Locate every Plasmodium falciparum-infected red blood cell.
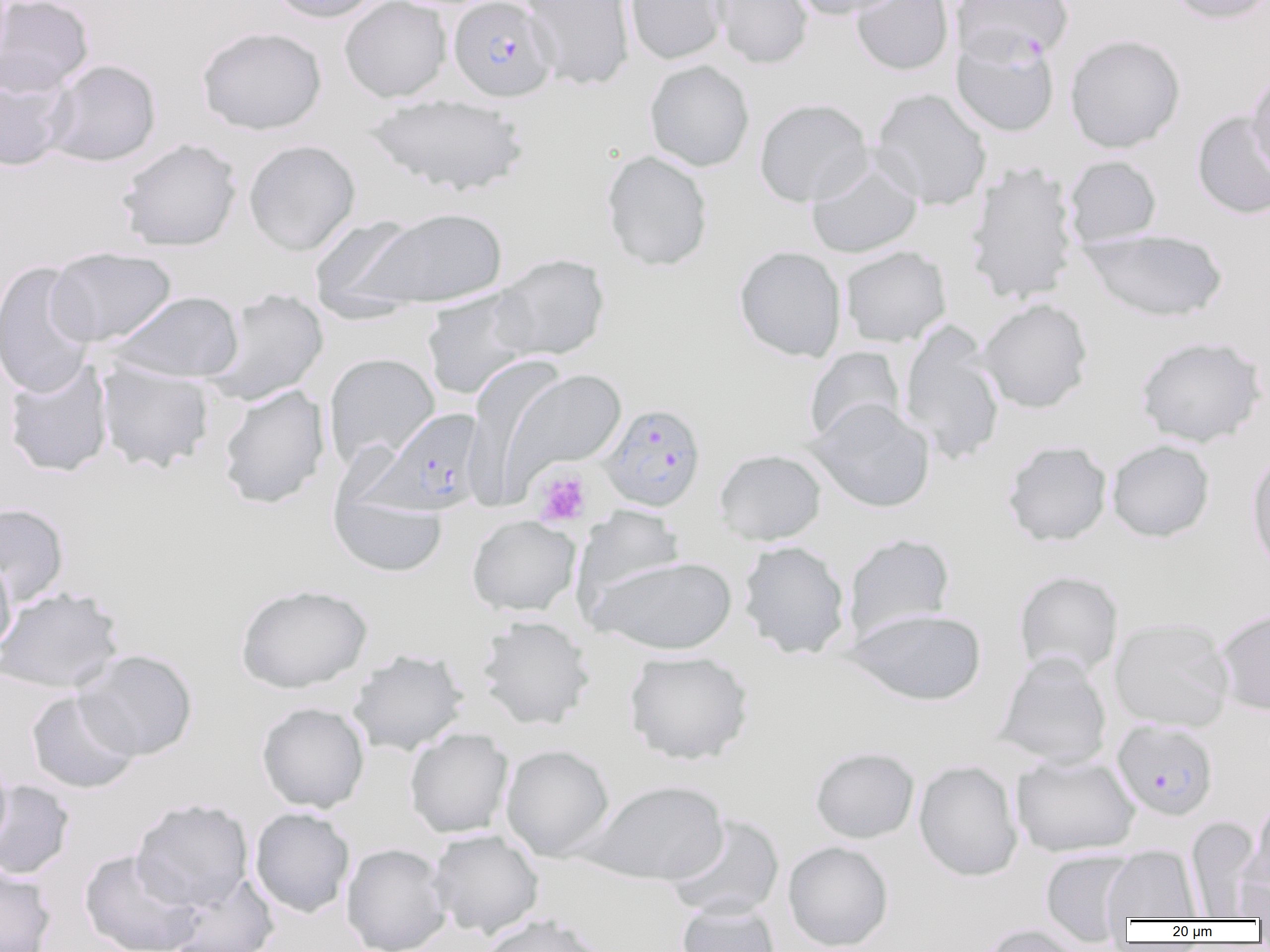

Approximate bounding boxes as (x1, y1, x2, y2) in pixels.
Plasmodium falciparum-infected red blood cells: (448, 0, 558, 102), (951, 30, 1060, 137), (598, 403, 707, 512), (368, 408, 487, 516), (1112, 719, 1219, 821).

{
  "slide_level_diagnosis": "Plasmodium falciparum",
  "platelet_locations": "approximate bounding boxes as (x1, y1, x2, y2) in pixels: (533, 468, 592, 526)",
  "magnification": "1000x",
  "image_size": "1270×952 pixels",
  "modality": "light microscopy",
  "field_of_view": "one of a larger specimen",
  "preparation": "thin blood smear",
  "uninfected_red_blood_cell_locations": "approximate bounding boxes as (x1, y1, x2, y2) in pixels: (0, 0, 94, 97), (266, 0, 383, 23), (339, 0, 452, 102), (522, 0, 636, 90), (623, 0, 730, 65), (711, 0, 814, 69), (788, 0, 907, 20), (851, 0, 954, 76), (952, 0, 1072, 49), (1164, 0, 1269, 25), (197, 26, 327, 135), (1065, 34, 1185, 152), (43, 59, 161, 167), (644, 60, 755, 171), (1246, 70, 1270, 181), (0, 71, 71, 171), (871, 88, 992, 211), (364, 94, 530, 196), (754, 98, 873, 207), (1192, 111, 1270, 219), (117, 137, 242, 251), (243, 140, 361, 255), (601, 150, 713, 271), (1064, 155, 1162, 247), (806, 156, 923, 258), (964, 160, 1080, 305), (358, 207, 508, 309), (309, 215, 426, 316), (1079, 228, 1229, 323), (840, 245, 952, 347), (734, 246, 847, 363), (45, 247, 177, 347), (491, 253, 610, 361), (0, 260, 97, 398), (206, 289, 329, 405), (420, 289, 536, 400), (108, 291, 244, 382), (978, 298, 1093, 413), (899, 322, 1006, 465), (1134, 335, 1268, 448), (804, 347, 906, 444), (323, 352, 440, 467), (461, 356, 566, 509), (3, 359, 114, 477), (95, 360, 216, 474), (506, 369, 628, 478), (217, 384, 330, 509), (807, 399, 935, 513), (1002, 440, 1113, 546), (1107, 440, 1214, 542), (1246, 447, 1270, 576), (713, 449, 827, 545), (330, 491, 448, 577), (0, 502, 70, 606), (572, 505, 686, 610), (466, 515, 581, 617), (843, 533, 955, 642), (738, 540, 851, 659), (608, 552, 743, 760), (0, 554, 16, 658), (588, 555, 737, 654), (1014, 571, 1123, 679), (235, 583, 372, 693), (0, 586, 124, 694), (844, 607, 987, 705), (1215, 607, 1270, 716), (476, 615, 595, 730), (1109, 617, 1234, 732), (347, 648, 469, 756), (75, 649, 198, 760), (623, 650, 754, 765), (995, 652, 1112, 768), (25, 690, 140, 794), (256, 702, 370, 813), (405, 728, 513, 838), (500, 744, 615, 861), (809, 746, 920, 844), (0, 753, 13, 854), (1011, 754, 1139, 857), (913, 760, 1023, 881), (582, 779, 729, 885), (0, 780, 75, 880), (1245, 793, 1270, 898), (130, 798, 254, 911), (250, 807, 356, 918), (666, 814, 785, 920), (1185, 816, 1262, 918), (428, 829, 544, 938), (783, 841, 894, 951), (341, 843, 451, 952), (1102, 845, 1201, 922), (80, 849, 203, 952), (1039, 849, 1138, 945), (0, 862, 57, 952), (164, 874, 280, 952), (676, 900, 781, 952), (477, 913, 611, 952), (975, 924, 1086, 952)"
}